Comment on the morphology of the erythrocytes.
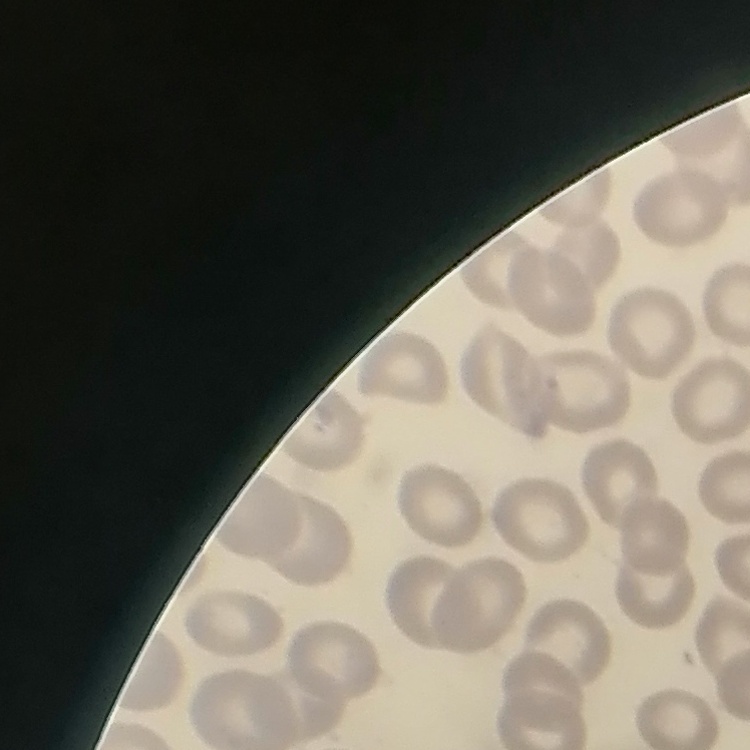
They show no rouleaux formation.

image_type: one tile cut from a larger photomicrograph
stain: Field's or Giemsa
preparation: thin blood film